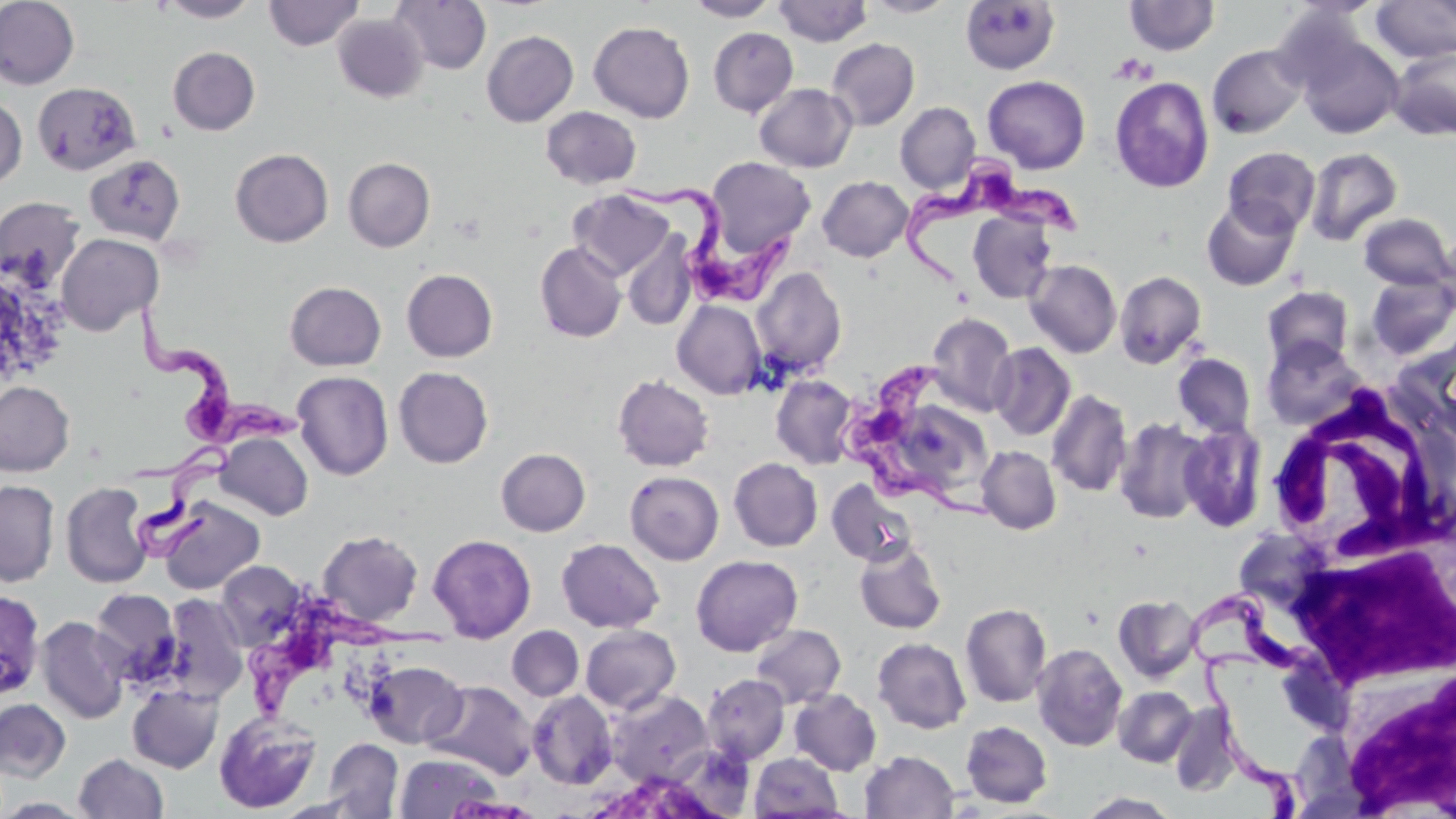
Summary:
  - Coordinate format: approximate bounding boxes as (x1,y1)-(x2,y2) corner pairs in pixels
  - Uninfected red blood cell locations: (0,0)-(80,89), (157,0)-(261,22), (263,0)-(364,50), (390,0)-(491,74), (685,0)-(780,21), (774,0)-(872,46), (861,0)-(961,18), (1124,0)-(1220,56), (1371,0)-(1456,63), (960,1)-(1059,74), (332,14)-(427,103), (588,21)-(695,122), (708,27)-(798,116), (482,30)-(578,127), (1295,32)-(1404,139), (826,38)-(920,130), (1207,44)-(1308,138), (168,46)-(260,135), (1388,46)-(1456,141), (983,75)-(1090,173), (1109,77)-(1215,193), (32,81)-(141,176), (754,83)-(857,172), (0,96)-(27,190), (895,102)-(980,193), (541,106)-(642,189), (1223,146)-(1320,236), (1304,147)-(1403,246), (230,148)-(333,247), (84,154)-(185,245), (343,157)-(435,252), (705,157)-(816,260), (818,176)-(913,261), (568,190)-(675,281), (0,197)-(86,292), (1202,197)-(1300,291), (968,210)-(1057,304), (1358,213)-(1454,290), (621,233)-(697,330), (55,234)-(162,335), (535,242)-(627,342), (1025,259)-(1122,358), (751,267)-(847,376), (401,268)-(498,362), (1114,271)-(1207,369), (1365,272)-(1456,360), (285,281)-(386,371), (1262,286)-(1354,370), (672,300)-(767,400), (926,313)-(1017,416), (1262,335)-(1365,431), (1397,340)-(1456,441), (989,342)-(1076,441), (1173,353)-(1256,438), (393,367)-(493,468), (292,371)-(394,480), (612,374)-(714,471), (771,374)-(859,469), (0,381)-(75,476), (1046,389)-(1132,497), (1114,417)-(1212,524), (1179,421)-(1268,532), (215,431)-(313,520), (976,446)-(1061,534), (496,448)-(591,536), (729,458)-(822,551), (625,470)-(724,565), (0,480)-(60,587), (827,480)-(916,566), (61,482)-(153,588), (157,497)-(265,595), (317,530)-(423,626), (428,533)-(536,642), (556,538)-(665,632), (853,538)-(947,634), (690,555)-(803,656), (216,560)-(306,648), (89,588)-(182,684), (0,589)-(45,700), (1113,594)-(1202,683), (162,595)-(248,703), (960,602)-(1052,707), (36,616)-(131,724), (750,624)-(846,708), (580,625)-(681,714), (507,626)-(584,701), (872,637)-(971,734), (1032,643)-(1128,751), (363,660)-(467,748), (701,673)-(790,764), (423,680)-(538,778), (127,684)-(223,773), (1113,686)-(1198,767), (606,689)-(714,787), (789,689)-(882,776), (527,690)-(618,789), (0,698)-(71,782), (1168,703)-(1241,797), (214,710)-(321,814), (961,720)-(1053,808), (323,737)-(404,818), (860,750)-(959,818), (395,752)-(502,818), (750,752)-(845,817), (74,753)-(169,818), (1076,791)-(1182,818), (0,798)-(95,818)
  - White blood cell locations: (1264,389)-(1452,566), (1289,537)-(1453,689), (1337,663)-(1455,815)
  - Platelet locations: (1108,53)-(1157,85)
  - Trypanosoma brucei locations: (902,149)-(1075,292), (619,176)-(798,313), (134,301)-(304,448), (842,372)-(993,509), (131,442)-(231,566), (1185,582)-(1335,691), (247,600)-(450,725), (1197,652)-(1310,819)
  - Slide-level diagnosis: Trypanosoma brucei
  - Field of view: single
  - Stain: May-Grünwald-Giemsa
  - Preparation: thin blood smear
  - Magnification: 1000x
  - Modality: optical microscopy
  - Image size: 1456×819 pixels